Assess the morphology of the red blood cells.
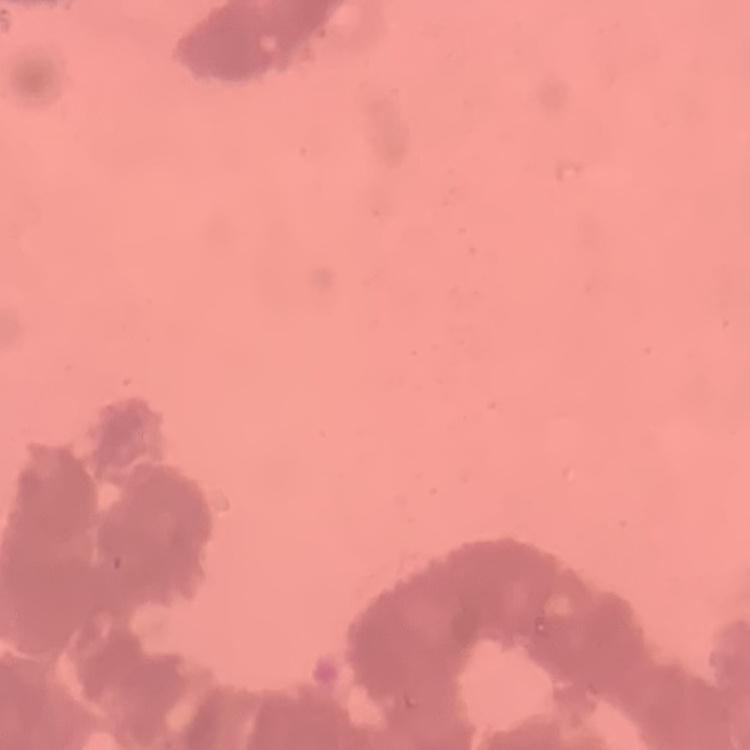

Rouleaux formation.

stain = Field's or Giemsa
preparation = thin blood smear
image type = square crop of a larger photomicrograph